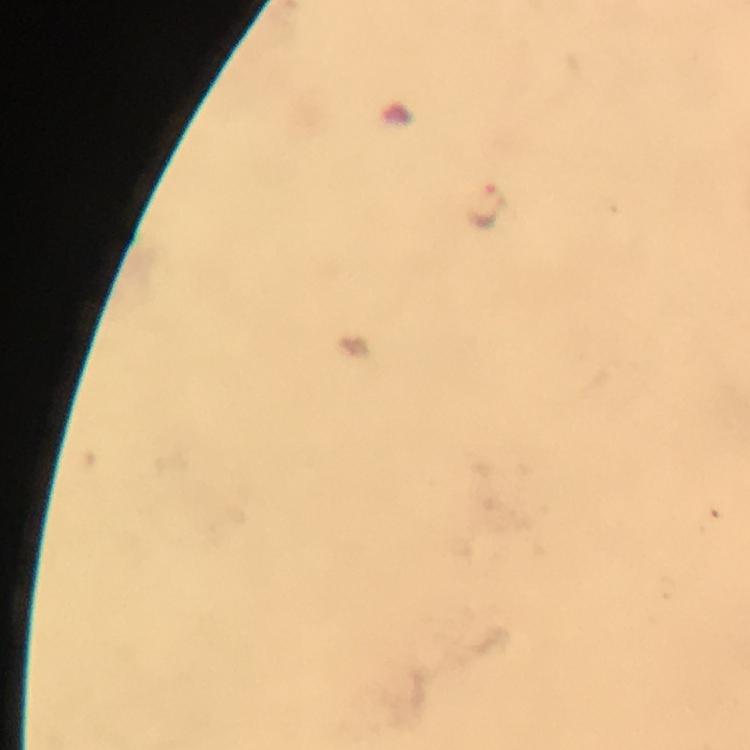 Approximate centers as {x, y} in pixels. Malaria parasite locations: {488, 207}. 100x magnification. Cropped region of a single field of view. From a malaria diagnostic workup. Photographed through the microscope with a smartphone camera. Immersion oil applied. Giemsa-stained preparation. Image is 750×750 pixels. Thick smear.